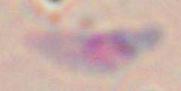 Toxoplasma gondii is shown. Micrograph. Captured at 1000x magnification.